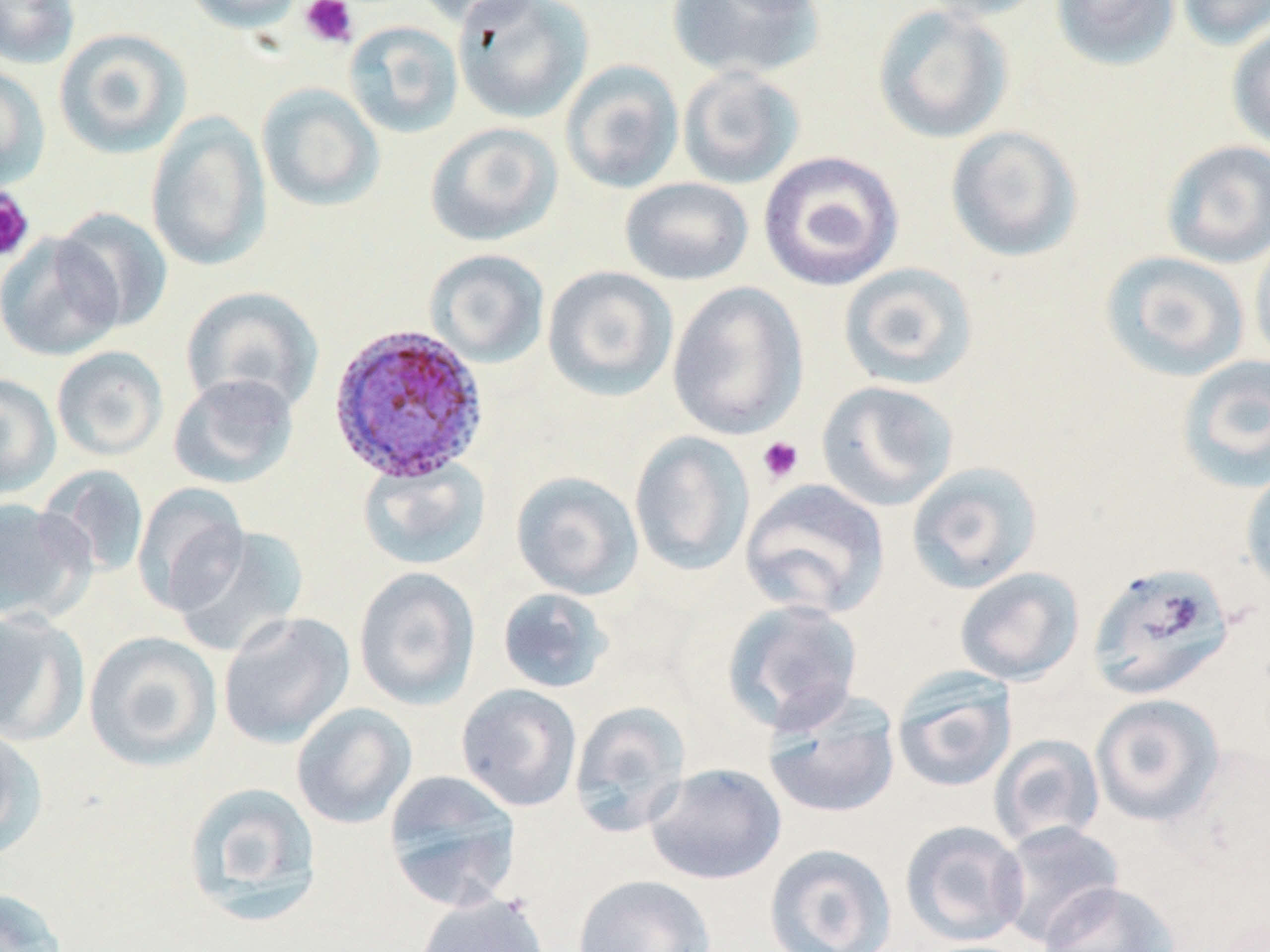

Approximate bounding boxes as (x1, y1, x2, y2) in pixels. Plasmodium ovale-infected red blood cell locations: (328, 323, 489, 485). Uninfected red blood cell locations: (0, 0, 80, 69), (182, 0, 308, 33), (411, 0, 544, 27), (452, 0, 594, 124), (665, 0, 825, 81), (916, 0, 1051, 23), (1050, 0, 1182, 71), (1175, 0, 1270, 51), (872, 4, 1014, 144), (343, 20, 464, 138), (1226, 24, 1270, 153), (53, 27, 192, 159), (560, 59, 684, 194), (0, 65, 50, 192), (676, 65, 805, 190), (256, 83, 385, 212), (145, 111, 271, 273), (424, 122, 564, 247), (945, 125, 1083, 262), (1160, 140, 1270, 268), (758, 150, 904, 292), (619, 177, 755, 286), (54, 207, 174, 332), (0, 231, 124, 361), (1249, 233, 1270, 369), (424, 249, 550, 369), (1099, 250, 1251, 382), (837, 262, 978, 390), (542, 266, 679, 402), (666, 281, 809, 440), (180, 286, 324, 417), (51, 346, 169, 461), (1175, 355, 1270, 492), (0, 373, 61, 500), (167, 373, 299, 489), (815, 380, 959, 512), (629, 431, 755, 577), (358, 457, 491, 571), (905, 460, 1043, 593), (1240, 464, 1270, 595), (38, 465, 150, 580), (510, 470, 644, 600), (739, 478, 891, 619), (132, 483, 250, 616), (0, 497, 93, 625), (172, 525, 309, 658), (1086, 561, 1236, 701), (353, 566, 481, 710), (954, 567, 1085, 686), (496, 587, 614, 694), (721, 598, 865, 734), (0, 608, 88, 744), (218, 611, 355, 749), (83, 630, 222, 771), (891, 669, 1018, 793), (455, 683, 583, 812), (762, 693, 901, 819), (1089, 693, 1226, 827), (568, 700, 690, 838), (291, 702, 417, 829), (0, 721, 44, 858), (989, 734, 1105, 849), (644, 762, 787, 884), (382, 769, 522, 910), (182, 781, 323, 927), (900, 820, 1030, 947), (992, 820, 1124, 948), (764, 843, 897, 952), (572, 874, 716, 952), (1037, 880, 1181, 952), (0, 886, 67, 952), (415, 893, 550, 952). Platelet locations: (300, 0, 358, 48), (0, 187, 34, 263), (756, 436, 804, 484). Slide-level diagnosis: Plasmodium ovale. Image is 1270×952 pixels. One field of a larger specimen. May-Grünwald-Giemsa-stained preparation. 1000x magnification. Optical microscopy. Thin blood film.